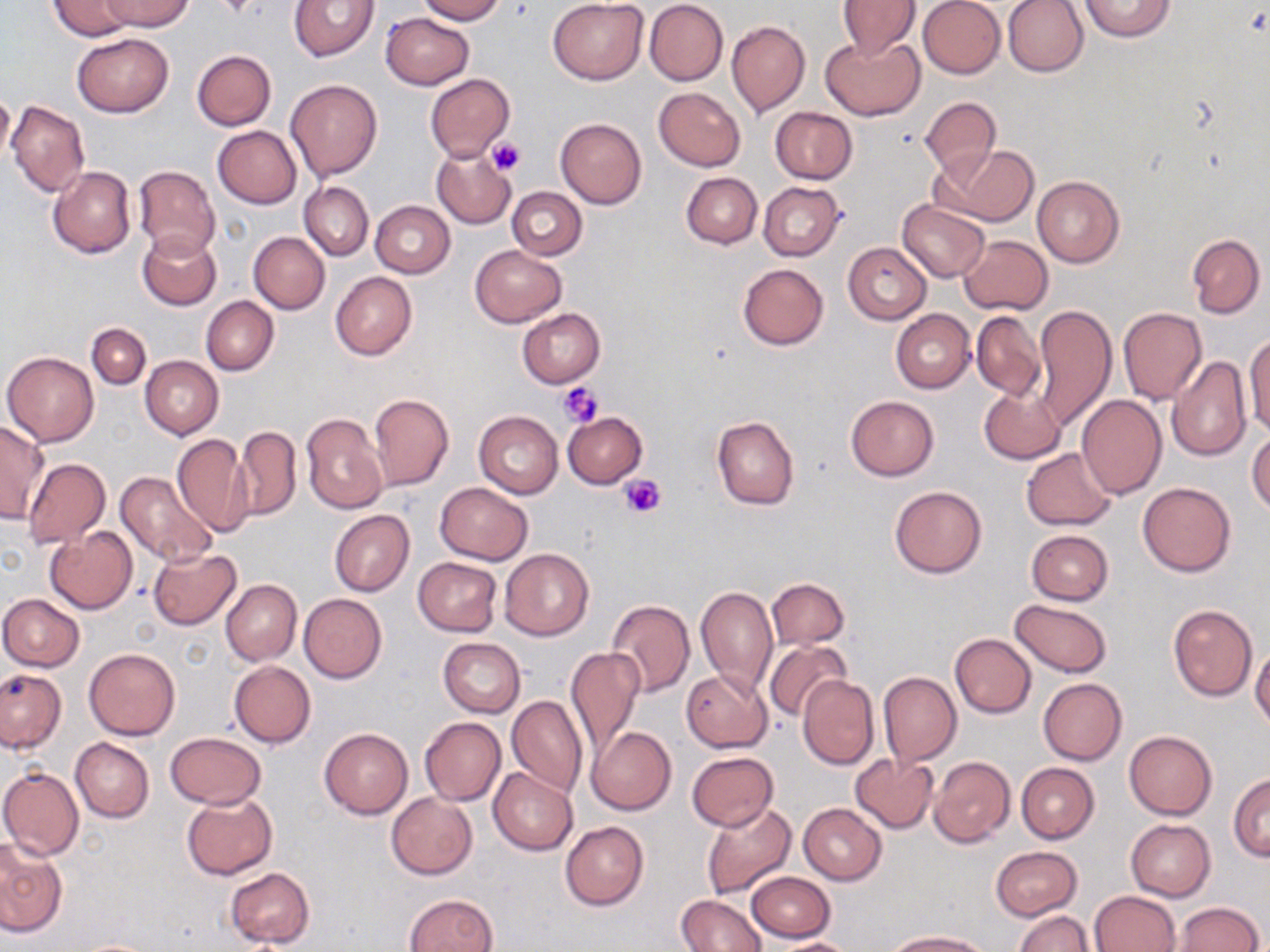

slide-level diagnosis = no evidence of blood parasites
preparation = thin blood film
magnification = 1000x
field of view = one of a larger specimen
uninfected red blood cell locations = approximate bounding boxes as [x1, y1, x2, y2] in pixels: [48, 0, 135, 39], [101, 0, 194, 31], [289, 0, 380, 62], [417, 0, 505, 23], [836, 0, 921, 61], [917, 0, 1006, 79], [1004, 0, 1089, 77], [1078, 0, 1176, 42], [547, 1, 649, 84], [644, 1, 728, 86], [380, 13, 474, 90], [727, 20, 810, 116], [72, 33, 173, 117], [822, 35, 924, 121], [191, 50, 275, 131], [425, 74, 514, 162], [286, 79, 382, 180], [654, 87, 745, 171], [1, 90, 15, 167], [919, 97, 1001, 176], [6, 99, 89, 197], [769, 107, 856, 184], [555, 117, 647, 209], [213, 126, 301, 208], [932, 144, 1039, 226], [432, 147, 515, 229], [133, 164, 220, 259], [48, 167, 135, 258], [681, 172, 762, 248], [1032, 175, 1124, 266], [300, 182, 374, 259], [758, 182, 844, 260], [507, 187, 586, 260], [370, 200, 454, 278], [898, 200, 990, 283], [137, 229, 220, 311], [249, 232, 330, 313], [959, 234, 1053, 315], [1187, 234, 1264, 317], [844, 243, 932, 323], [470, 244, 566, 326], [738, 263, 828, 350], [330, 271, 417, 359], [201, 296, 278, 375], [1031, 305, 1116, 430], [517, 307, 605, 387], [1118, 307, 1207, 405], [891, 310, 974, 394], [971, 311, 1045, 399], [86, 323, 150, 388], [1245, 334, 1270, 440], [2, 351, 99, 447], [140, 355, 223, 439], [1167, 356, 1252, 462], [979, 384, 1065, 465], [369, 393, 454, 492], [1076, 394, 1167, 500], [846, 396, 938, 481], [473, 410, 563, 499], [563, 412, 648, 489], [301, 413, 389, 514], [711, 415, 800, 510], [0, 420, 46, 525], [231, 425, 302, 521], [1248, 430, 1270, 516], [172, 434, 252, 537], [156, 438, 247, 611], [1021, 448, 1116, 529], [23, 458, 111, 548], [116, 470, 218, 568], [1138, 482, 1235, 577], [435, 483, 531, 564], [889, 486, 987, 579], [328, 510, 414, 596], [45, 528, 137, 613], [1026, 530, 1113, 605], [499, 548, 594, 641], [148, 549, 241, 630], [413, 558, 501, 637], [767, 578, 848, 650], [221, 579, 301, 666], [696, 586, 778, 697], [0, 593, 83, 671], [299, 594, 387, 683], [607, 598, 695, 697], [1011, 598, 1112, 675], [1168, 604, 1256, 701], [949, 633, 1036, 717], [437, 637, 525, 717], [764, 638, 852, 723], [1250, 644, 1270, 731], [567, 647, 643, 758], [84, 648, 180, 740], [229, 661, 316, 746], [0, 668, 65, 753], [682, 670, 772, 752], [878, 671, 961, 765], [798, 675, 878, 770], [1038, 678, 1127, 764], [512, 682, 651, 794], [507, 696, 587, 798], [420, 717, 506, 805], [587, 727, 676, 815], [320, 728, 413, 819], [1124, 730, 1218, 819], [165, 732, 267, 809], [71, 738, 153, 823], [688, 751, 778, 831], [851, 753, 939, 833], [929, 756, 1014, 848], [1016, 762, 1100, 843], [0, 767, 84, 861], [489, 767, 578, 855], [1229, 774, 1270, 860], [181, 793, 277, 881], [386, 793, 478, 880], [701, 800, 796, 900], [799, 804, 886, 885], [1126, 819, 1216, 902], [561, 821, 649, 910], [0, 837, 67, 938], [990, 846, 1082, 922], [225, 867, 314, 948], [745, 871, 835, 942], [1090, 891, 1181, 952], [403, 893, 498, 952], [677, 894, 766, 951], [1170, 902, 1263, 951], [1014, 911, 1094, 952], [889, 931, 991, 951], [770, 938, 858, 952]
image size = 1270×952 pixels
modality = light microscopy
stain = May-Grünwald-Giemsa
platelet locations = approximate bounding boxes as [x1, y1, x2, y2] in pixels: [486, 137, 525, 176], [558, 381, 605, 429], [618, 476, 664, 518]